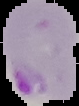

image size = 79×106 pixels
result = malaria parasites identified
preparation = thin blood smear
image type = segmented cell region on a black background